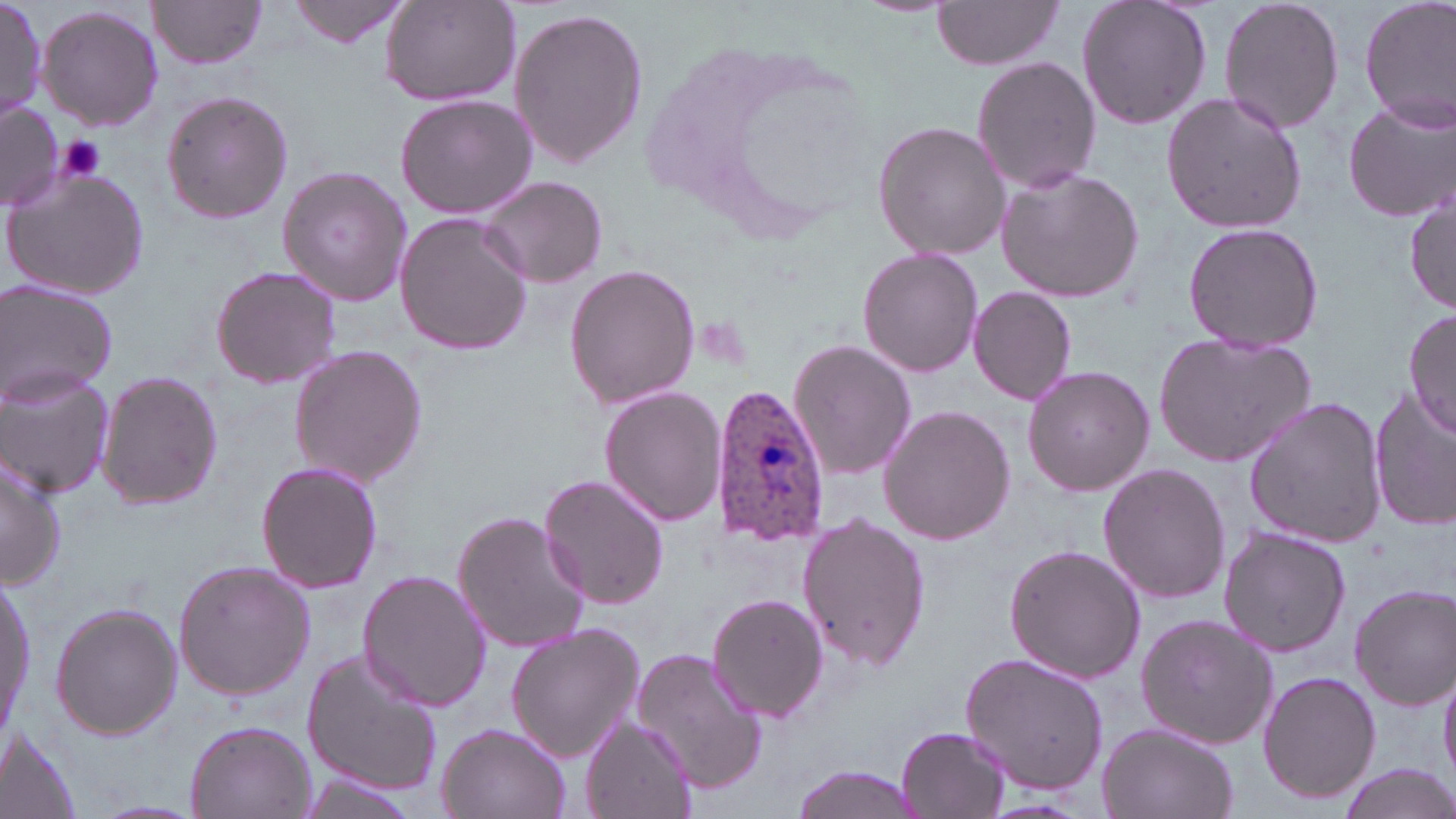

Summary:
  - Coordinate format: approximate bounding boxes as [x1, y1, x2, y2] in pixels
  - Plasmodium ovale-infected red blood cell locations: [710, 386, 831, 548]
  - Uninfected red blood cell locations: [149, 0, 269, 71], [289, 0, 411, 48], [379, 0, 520, 106], [1075, 0, 1212, 131], [1217, 0, 1346, 136], [1358, 0, 1456, 133], [0, 1, 47, 120], [930, 1, 1066, 71], [37, 4, 164, 133], [508, 6, 649, 170], [972, 56, 1100, 194], [160, 90, 294, 224], [1160, 90, 1308, 235], [393, 94, 537, 219], [1343, 97, 1454, 224], [0, 102, 60, 210], [873, 121, 1010, 260], [2, 165, 153, 303], [276, 165, 414, 309], [995, 167, 1145, 303], [479, 175, 609, 288], [1407, 186, 1455, 315], [396, 213, 530, 356], [1181, 221, 1323, 355], [857, 247, 985, 378], [563, 262, 701, 410], [209, 264, 343, 390], [0, 279, 118, 406], [968, 286, 1078, 405], [1404, 307, 1456, 443], [1152, 330, 1317, 469], [788, 339, 917, 481], [287, 345, 427, 487], [1021, 364, 1155, 498], [0, 367, 115, 498], [95, 369, 224, 510], [600, 387, 729, 525], [1368, 389, 1455, 531], [1243, 396, 1389, 548], [877, 404, 1016, 546], [2, 445, 67, 587], [256, 460, 383, 595], [1099, 462, 1230, 604], [538, 471, 671, 610], [453, 509, 591, 656], [798, 511, 931, 672], [1218, 526, 1352, 657], [1003, 542, 1145, 685], [173, 560, 315, 699], [3, 565, 36, 746], [357, 570, 490, 712], [1349, 583, 1455, 710], [707, 593, 828, 723], [50, 601, 183, 740], [1135, 614, 1280, 749], [505, 622, 644, 764], [631, 647, 772, 794], [302, 649, 444, 798], [958, 652, 1108, 797], [1439, 661, 1456, 786], [1256, 669, 1381, 805], [581, 716, 695, 819], [185, 719, 315, 819], [1096, 722, 1239, 819], [895, 723, 1012, 818], [438, 724, 570, 819], [0, 732, 83, 819], [1334, 764, 1456, 819], [787, 765, 926, 819], [298, 776, 412, 817]
  - Platelet locations: [56, 137, 108, 184]
  - Slide-level diagnosis: Plasmodium ovale
  - Image size: 1456×819 pixels
  - Field of view: one of a larger specimen
  - Stain: May-Grünwald-Giemsa
  - Modality: optical microscopy
  - Preparation: thin blood film
  - Magnification: 1000x